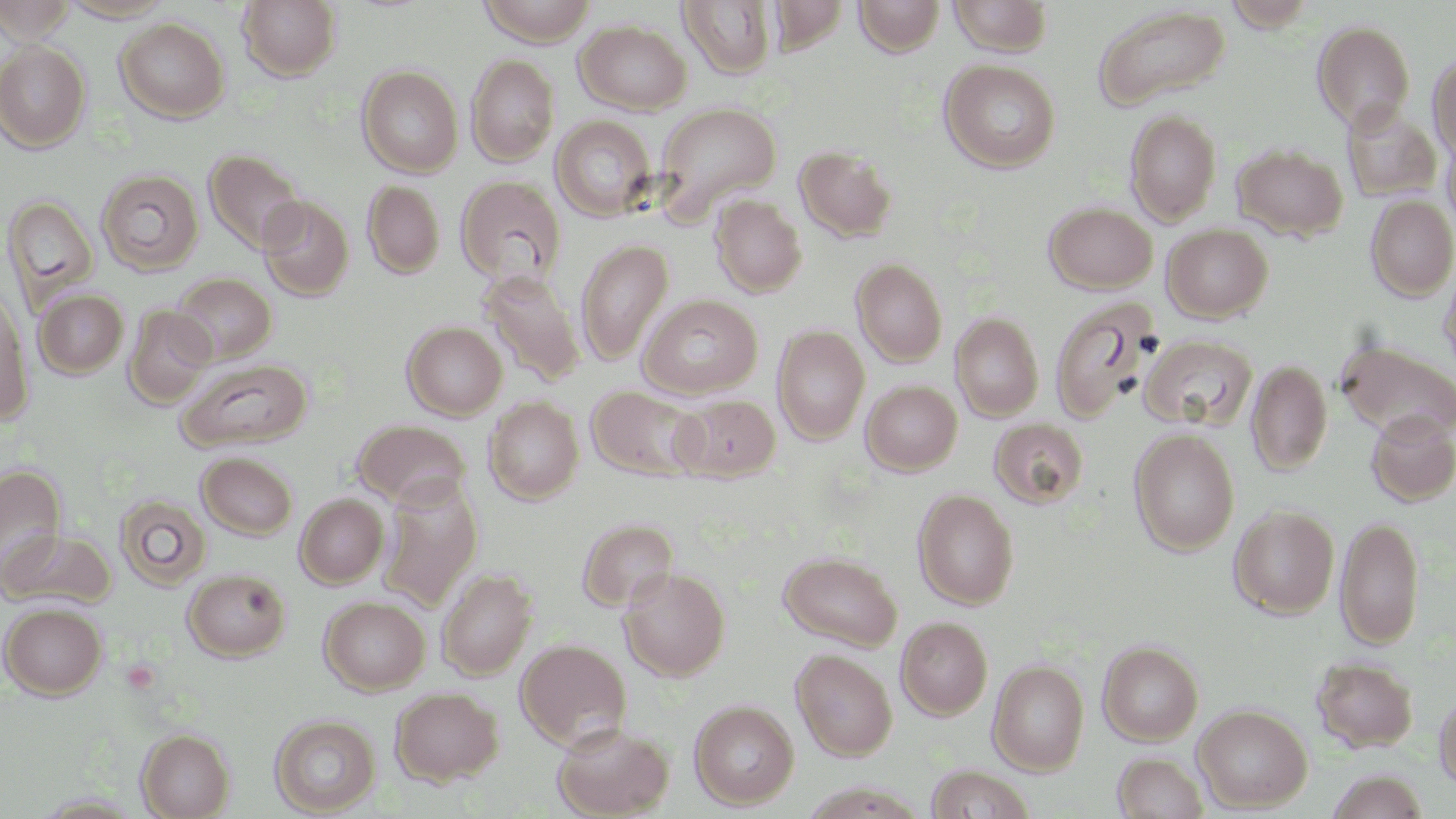 Approximate bounding boxes as (x1,y1)-(x2,y2) corner pairs in pixels. Uninfected red blood cell locations: (0,0)-(76,43), (58,0)-(175,22), (767,0)-(851,54), (854,0)-(945,57), (948,0)-(1054,56), (1223,0)-(1318,31), (238,1)-(342,81), (477,1)-(600,45), (678,1)-(777,79), (1093,4)-(1231,110), (115,17)-(229,123), (575,20)-(692,114), (1312,20)-(1415,131), (0,42)-(91,152), (1428,53)-(1456,161), (466,54)-(559,167), (940,59)-(1061,173), (357,65)-(463,177), (653,102)-(782,217), (1341,104)-(1443,201), (1125,109)-(1221,225), (550,115)-(656,222), (1441,130)-(1456,234), (1231,143)-(1348,241), (794,144)-(897,242), (203,149)-(308,254), (96,169)-(204,275), (456,175)-(566,287), (362,180)-(445,279), (710,194)-(807,297), (1366,194)-(1456,301), (3,195)-(99,312), (258,195)-(355,301), (1043,202)-(1158,294), (1161,223)-(1273,322), (576,239)-(673,366), (1439,253)-(1456,381), (851,258)-(948,366), (479,268)-(585,388), (172,272)-(276,364), (0,286)-(34,425), (34,288)-(129,378), (638,295)-(763,399), (1049,296)-(1162,422), (124,305)-(217,408), (950,312)-(1044,421), (402,321)-(507,420), (772,325)-(870,445), (1139,334)-(1258,431), (1335,339)-(1456,443), (178,358)-(312,451), (1246,358)-(1332,476), (861,379)-(962,475), (587,385)-(706,481), (673,394)-(781,481), (483,397)-(584,504), (1364,411)-(1456,505), (989,418)-(1088,508), (353,419)-(471,508), (1129,427)-(1239,556), (197,452)-(298,539), (0,464)-(66,581), (379,478)-(482,610), (913,488)-(1019,609), (295,493)-(388,588), (115,495)-(212,590), (1228,504)-(1339,618), (1335,514)-(1424,650), (577,518)-(679,613), (2,529)-(116,610), (778,551)-(903,651), (619,566)-(730,681), (182,568)-(291,661), (437,568)-(537,680), (319,596)-(430,695), (1,603)-(106,698), (896,616)-(992,720), (516,638)-(631,749), (1098,640)-(1203,746), (791,648)-(897,761), (1310,656)-(1419,752), (987,660)-(1089,775), (390,686)-(504,785), (1434,691)-(1456,790), (689,700)-(799,809), (1193,704)-(1312,812), (270,713)-(381,815), (552,722)-(674,819), (136,729)-(234,818), (1112,752)-(1209,818), (925,765)-(1035,819), (1326,770)-(1430,818). Slide-level diagnosis: no evidence of blood parasites. Image is 1456×819 pixels. May-Grünwald-Giemsa stain. Captured at 1000x magnification. Thin blood smear. Light microscopy. One field of a larger specimen.